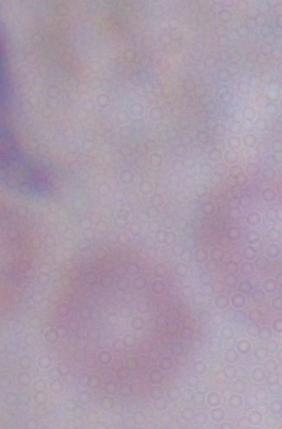
A trypanosome is seen. Micrograph. 1000x magnification.